Identify the cell.
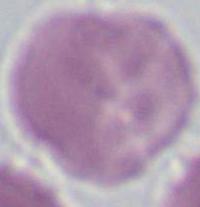

An erythrocyte.

{
  "magnification": "1000x",
  "modality": "photomicrograph"
}